Assess the morphology of the red blood cells.
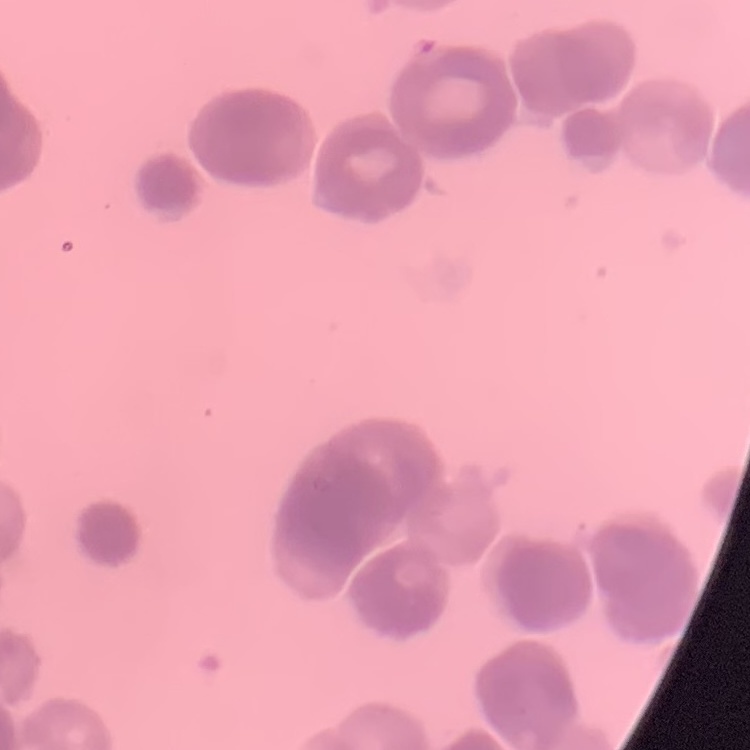

They show rouleaux formation.

image type = one tile cut from a larger photomicrograph
stain = Field's or Giemsa
preparation = thin blood film